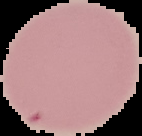

Summary:
  - Image size: 142×136 pixels
  - Malaria status: uninfected
  - Preparation: thin blood film
  - Image type: cell region segmented out of the field of view; surrounding area masked to black